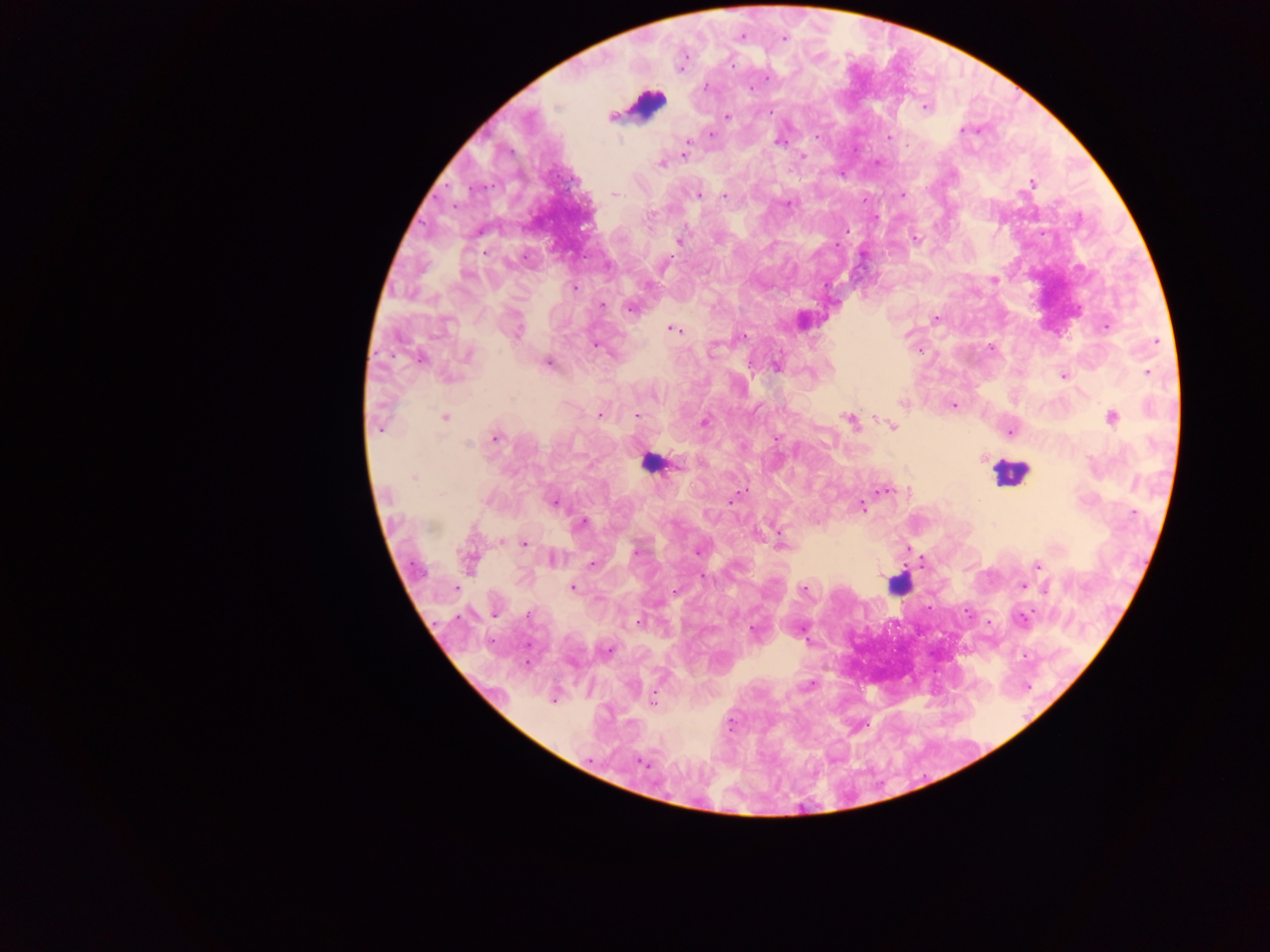

Approximate centers as x y in pixels. Plasmodium parasite locations: 742 36; 784 38; 705 87; 925 108; 727 116; 963 129; 711 134; 816 136; 889 136; 778 142; 688 143; 685 154; 803 156; 661 165; 1032 183; 615 194; 698 195; 902 195; 724 196; 789 205; 916 238; 679 240; 466 276; 993 280; 574 287; 602 304; 631 308; 935 319; 1106 326; 674 329; 516 331; 743 337; 1156 342; 596 346; 990 348; 920 350; 468 355; 420 359; 549 364; 777 366; 1148 372; 1063 375; 448 379; 904 403; 954 405; 599 415; 636 416; 1112 417; 445 418; 849 420; 704 422; 892 427; 378 429; 1010 432; 496 437; 468 444; 414 477; 884 491; 733 499; 554 502; 861 506; 1133 513; 582 523; 502 543; 524 543; 781 545; 697 551; 636 552; 553 559; 469 562; 592 563; 1037 565; 705 578; 1022 586; 572 587; 455 588; 1046 589; 803 590; 676 592; 495 615; 529 616; 1022 618; 637 622; 754 629; 608 650; 809 686; 652 699; 553 700; 642 763. Leukocyte locations: 646 104; 650 464; 1009 473; 899 584. Photographed through a microscope with a mobile-phone camera. Single field of view. Thick blood smear. Sample from Ghana. Image is 1270×952 pixels.